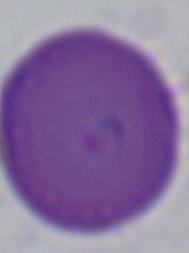

Summary:
  - Magnification: 1000x
  - Modality: photomicrograph
  - Identification: Babesia